Comment on the morphology of the red blood cells.
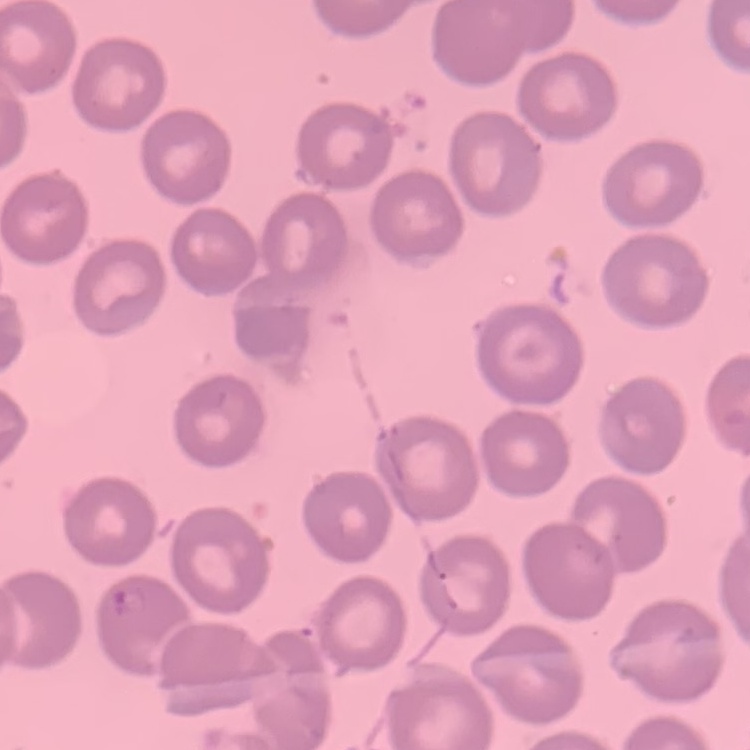
No rouleaux formation.

Summary:
  - Image type: square crop of a larger photomicrograph
  - Stain: Field's or Giemsa
  - Preparation: thin peripheral smear